Identify the preparation type.
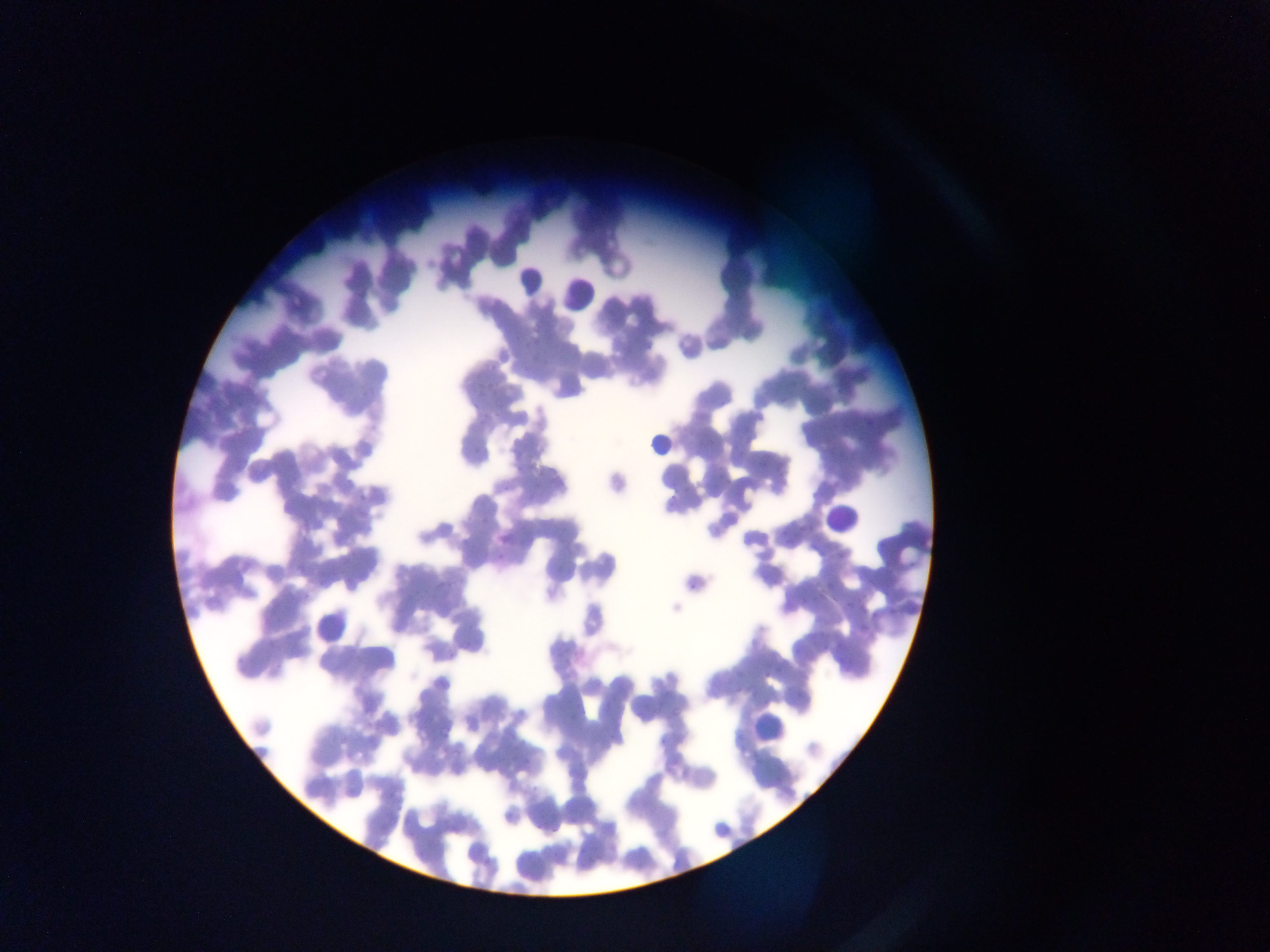

Thin blood smear.

capture = mobile-phone photograph through a microscope
Plasmodium parasite locations = approximate bounding boxes as left top right bottom in pixels: 474 388 486 398; 480 414 490 422; 863 419 871 425; 344 474 357 488; 358 493 368 501; 337 513 345 523; 477 513 492 525; 495 550 507 560; 690 579 697 591; 844 601 854 611; 857 627 868 637; 266 639 277 648; 821 641 831 650; 763 672 769 680; 733 686 742 696; 670 705 681 718
image size = 1270×952 pixels
country = Ghana
field of view = single
leukocyte locations = approximate bounding boxes as left top right bottom in pixels: 512 266 548 296; 558 278 590 315; 644 437 673 457; 818 493 866 542; 753 704 794 743